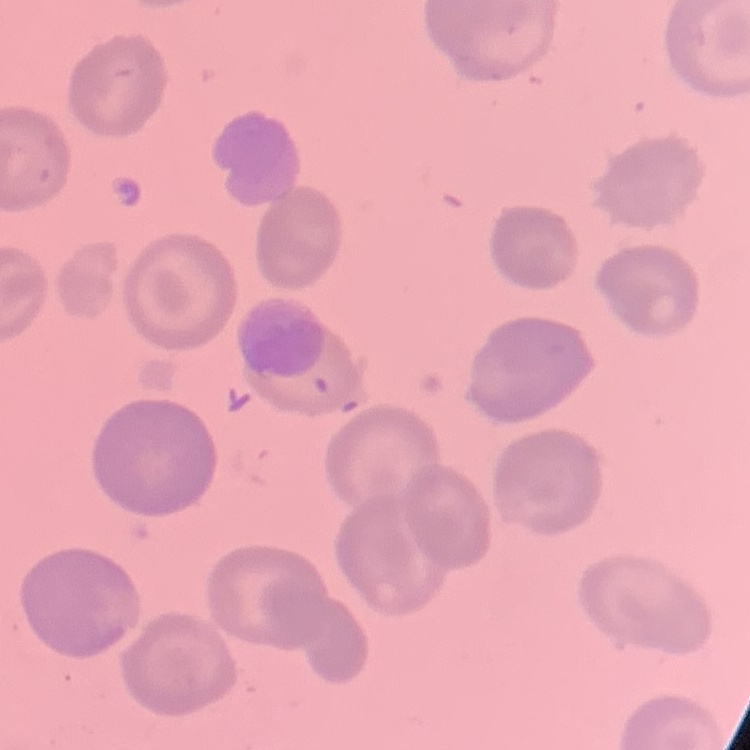

Summary:
  - Erythrocyte morphology: no rouleaux formation
  - Image type: one tile cut from a larger photomicrograph
  - Stain: Field's or Giemsa
  - Preparation: thin blood smear